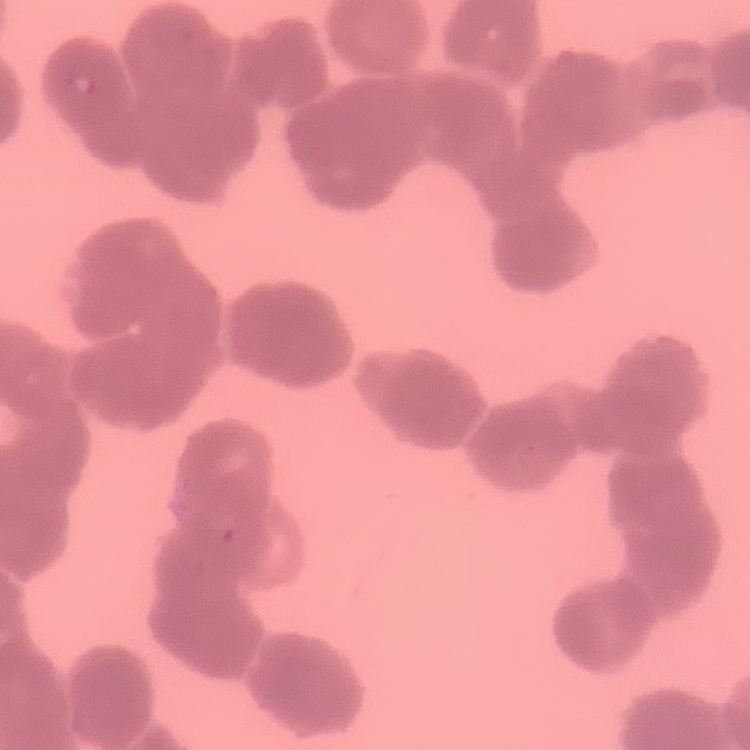
{
  "red_blood_cell_morphology": "rouleaux formation",
  "preparation": "thin peripheral smear",
  "stain": "Field's or Giemsa",
  "image_type": "one tile cut from a larger photomicrograph"
}